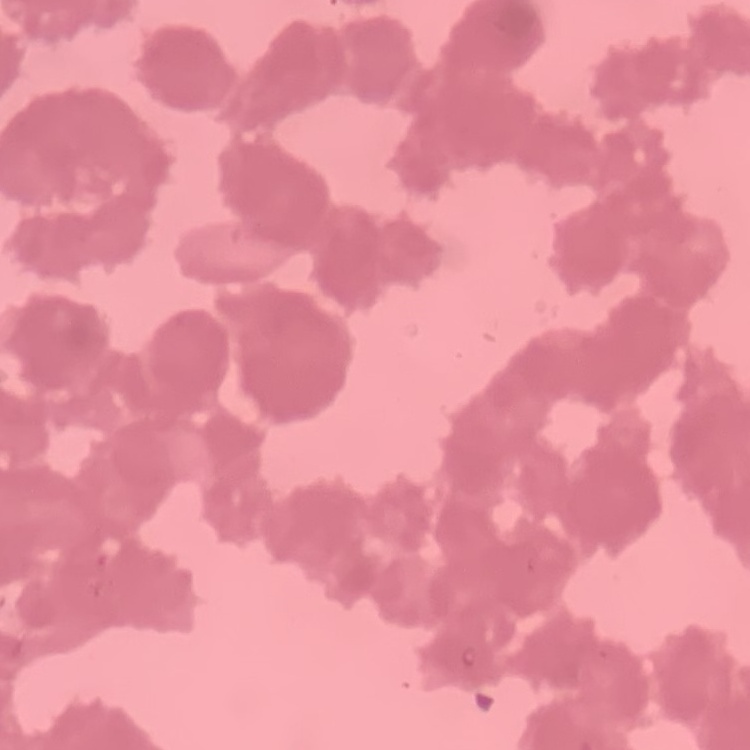

red blood cell morphology = rouleaux formation
preparation = thin peripheral smear
stain = Field's or Giemsa
image type = one tile cut from a larger photomicrograph